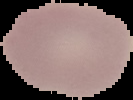

Malaria status: uninfected. Image is 133×100 pixels. From a thin blood film. Cell region segmented out of the field of view; the surrounding area is masked to black.